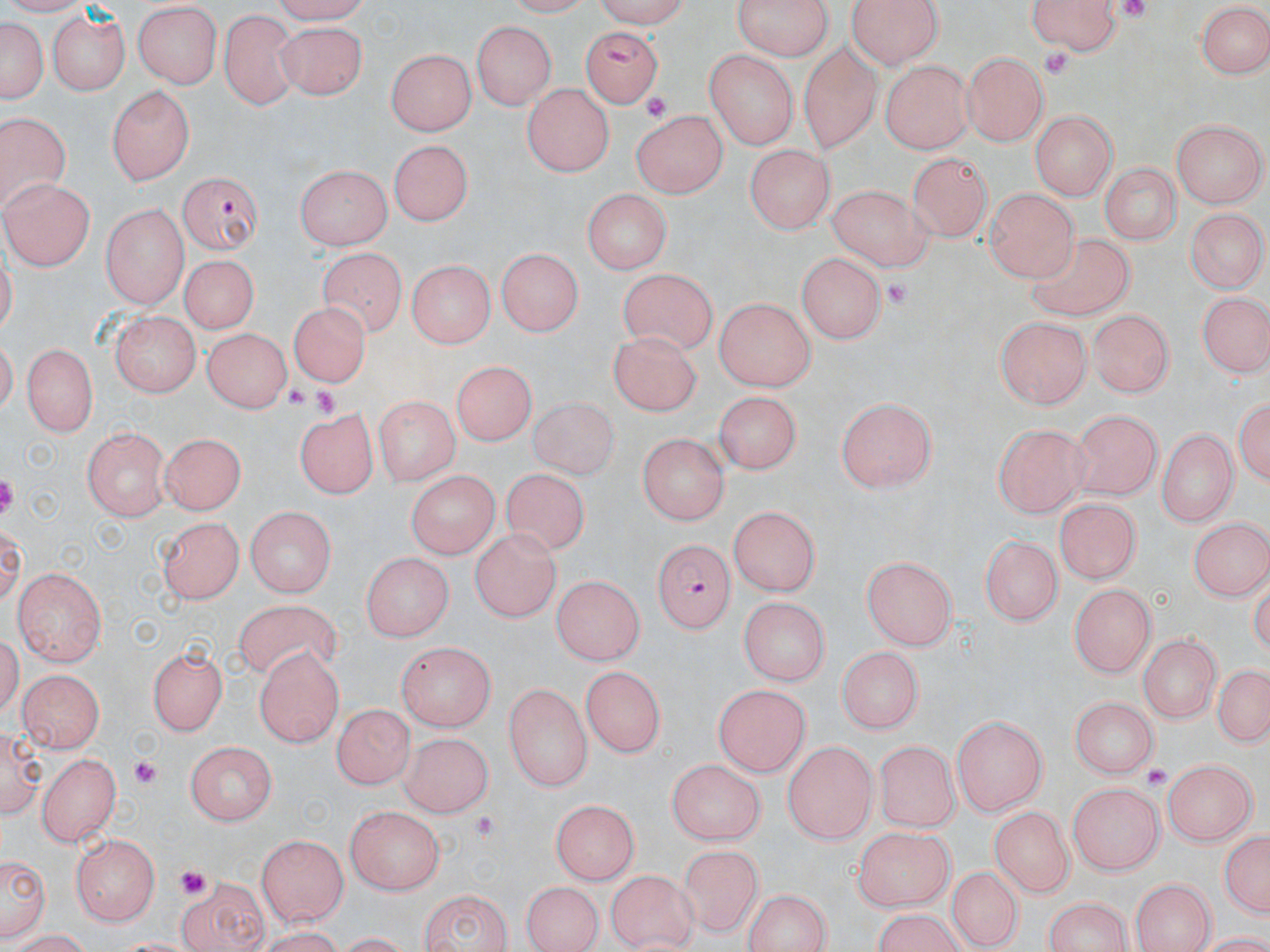

Approximate bounding boxes as (x1, y1, x2, y2) in pixels. Plasmodium falciparum-infected red blood cell locations: (582, 25, 662, 103), (177, 171, 263, 254), (650, 540, 734, 634). Platelet locations: (1118, 0, 1153, 25), (1040, 46, 1076, 84), (641, 91, 673, 123), (879, 277, 918, 308), (282, 382, 308, 411), (311, 385, 340, 418), (132, 757, 161, 790), (1144, 766, 1171, 793), (471, 815, 493, 839), (179, 869, 207, 897). Uninfected red blood cell locations: (120, 0, 208, 157), (587, 0, 694, 26), (728, 0, 836, 60), (845, 0, 943, 69), (1024, 0, 1123, 54), (1196, 3, 1268, 78), (134, 4, 221, 87), (44, 10, 127, 95), (221, 11, 300, 110), (1, 14, 49, 110), (471, 19, 556, 110), (277, 20, 366, 101), (799, 44, 881, 150), (388, 46, 476, 133), (704, 50, 795, 149), (965, 51, 1046, 145), (882, 61, 970, 154), (106, 83, 195, 187), (521, 85, 614, 176), (1031, 108, 1115, 200), (631, 110, 724, 200), (1, 113, 69, 221), (1172, 120, 1262, 206), (389, 138, 477, 222), (746, 142, 837, 233), (908, 151, 994, 235), (1099, 162, 1178, 249), (293, 165, 394, 246), (6, 177, 95, 269), (824, 184, 930, 269), (582, 187, 668, 277), (984, 187, 1077, 281), (103, 202, 188, 304), (1186, 206, 1266, 293), (1026, 230, 1141, 329), (319, 245, 405, 336), (498, 246, 584, 333), (795, 253, 889, 347), (178, 255, 256, 336), (402, 261, 496, 350), (619, 268, 718, 360), (1198, 296, 1268, 378), (714, 299, 814, 393), (288, 304, 373, 386), (1091, 308, 1173, 399), (108, 313, 200, 398), (994, 315, 1092, 407), (203, 324, 291, 411), (607, 331, 703, 416), (22, 343, 96, 437), (448, 363, 532, 452), (1234, 388, 1268, 490), (719, 391, 806, 471), (835, 393, 940, 492), (373, 396, 457, 490), (526, 397, 627, 483), (292, 409, 375, 502), (1072, 410, 1159, 501), (992, 419, 1086, 515), (1155, 426, 1239, 525), (84, 427, 173, 520), (158, 433, 245, 517), (639, 433, 729, 524), (499, 467, 597, 557), (404, 470, 496, 558), (1054, 501, 1142, 584), (729, 506, 818, 598), (244, 509, 338, 596), (1188, 514, 1270, 601), (156, 517, 243, 606), (468, 528, 558, 622), (979, 535, 1061, 625), (359, 552, 452, 645), (864, 556, 958, 650), (14, 567, 109, 667), (549, 574, 645, 667), (1068, 581, 1157, 673), (737, 597, 829, 685), (234, 602, 341, 677), (1139, 634, 1217, 727), (146, 639, 229, 735), (392, 642, 498, 731), (836, 644, 922, 735), (256, 648, 344, 746), (1210, 661, 1269, 752), (582, 666, 667, 755), (19, 669, 104, 754), (504, 681, 591, 793), (713, 682, 807, 775), (1070, 695, 1159, 775), (330, 702, 414, 789), (954, 714, 1048, 815), (398, 732, 490, 818), (876, 737, 960, 829), (182, 740, 276, 827), (781, 741, 877, 843), (41, 751, 120, 846), (669, 757, 766, 846), (1164, 759, 1256, 845), (1064, 784, 1164, 872), (548, 798, 643, 882), (345, 807, 443, 896), (993, 809, 1073, 896), (1218, 825, 1270, 921), (856, 828, 953, 913), (256, 832, 351, 926), (71, 834, 158, 927), (674, 845, 765, 937), (1, 851, 49, 945), (943, 863, 1025, 951), (607, 871, 699, 950), (175, 875, 274, 952), (1131, 876, 1214, 952), (520, 879, 603, 952), (743, 888, 832, 952), (415, 890, 515, 951), (1039, 894, 1135, 952), (4, 926, 98, 951). Slide-level diagnosis: Plasmodium falciparum. Captured at 1000x magnification. May-Grünwald-Giemsa stain. Thin blood smear. Image is 1270×952 pixels. One field of a larger specimen. Optical microscopy.